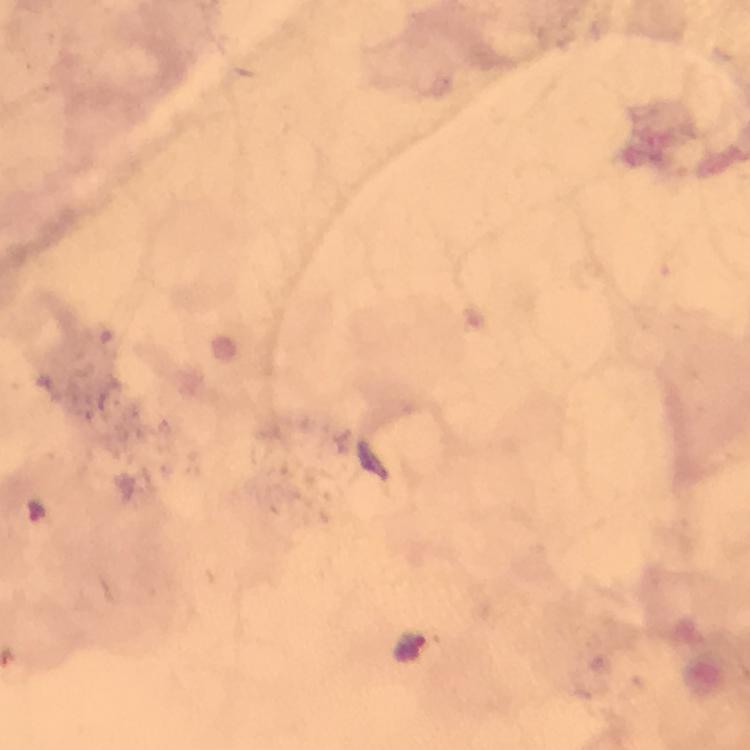 Approximate centers as {x, y} in pixels. Malaria parasite locations: {412, 649}. Immersion oil applied. 100x magnification. A crop from one field of view. Image is 750×750 pixels. Giemsa stain. From a malaria diagnostic workup. Thick blood smear. Photographed with a smartphone mounted on the microscope.